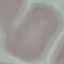
malaria status = uninfected
stain = Giemsa
preparation = thin smear
capture = smartphone camera at the microscope eyepiece
image type = automatically extracted cell patch, resized to 64 × 64 pixels